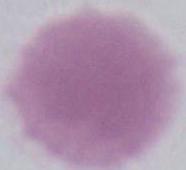
Summary:
  - Magnification: 1000x
  - Identification: red blood cell
  - Modality: micrograph